State which parasite is depicted.
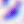

This is Toxoplasma gondii.

Summary:
  - Magnification: 400x
  - Modality: photomicrograph